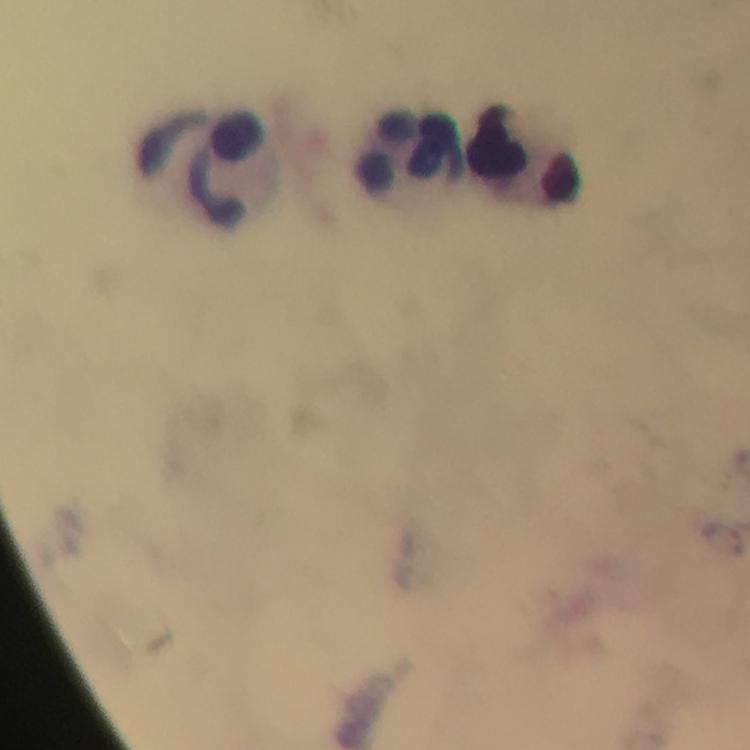

Approximate centers as (x, y) in pixels.
Summary:
  - Plasmodium parasite locations: (723, 542)
  - Leukocyte locations: (407, 151), (522, 152), (201, 165)
  - Context: from a diagnostic examination for malaria
  - Preparation: thick smear
  - Image size: 750×750 pixels
  - Magnification: 100x
  - Immersion oil: applied
  - Cropped from: a single field of view
  - Capture: smartphone mounted on the microscope
  - Stain: Giemsa